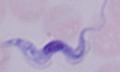

Micrograph. Captured at 1000x magnification. A trypanosome is shown.